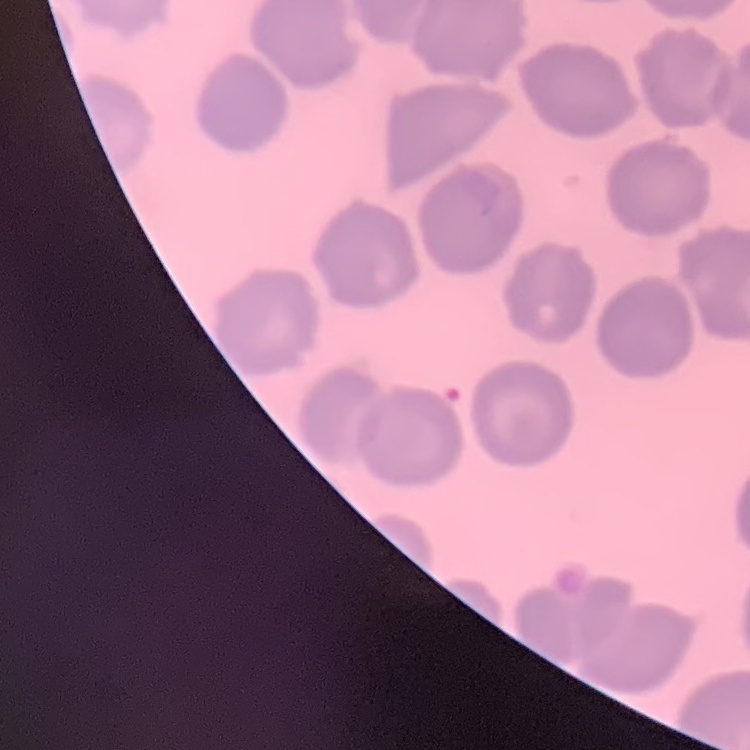
Summary:
  - Erythrocyte morphology: no rouleaux formation
  - Image type: one tile cut from a larger photomicrograph
  - Preparation: thin peripheral smear
  - Stain: Field's or Giemsa